Report the malaria status.
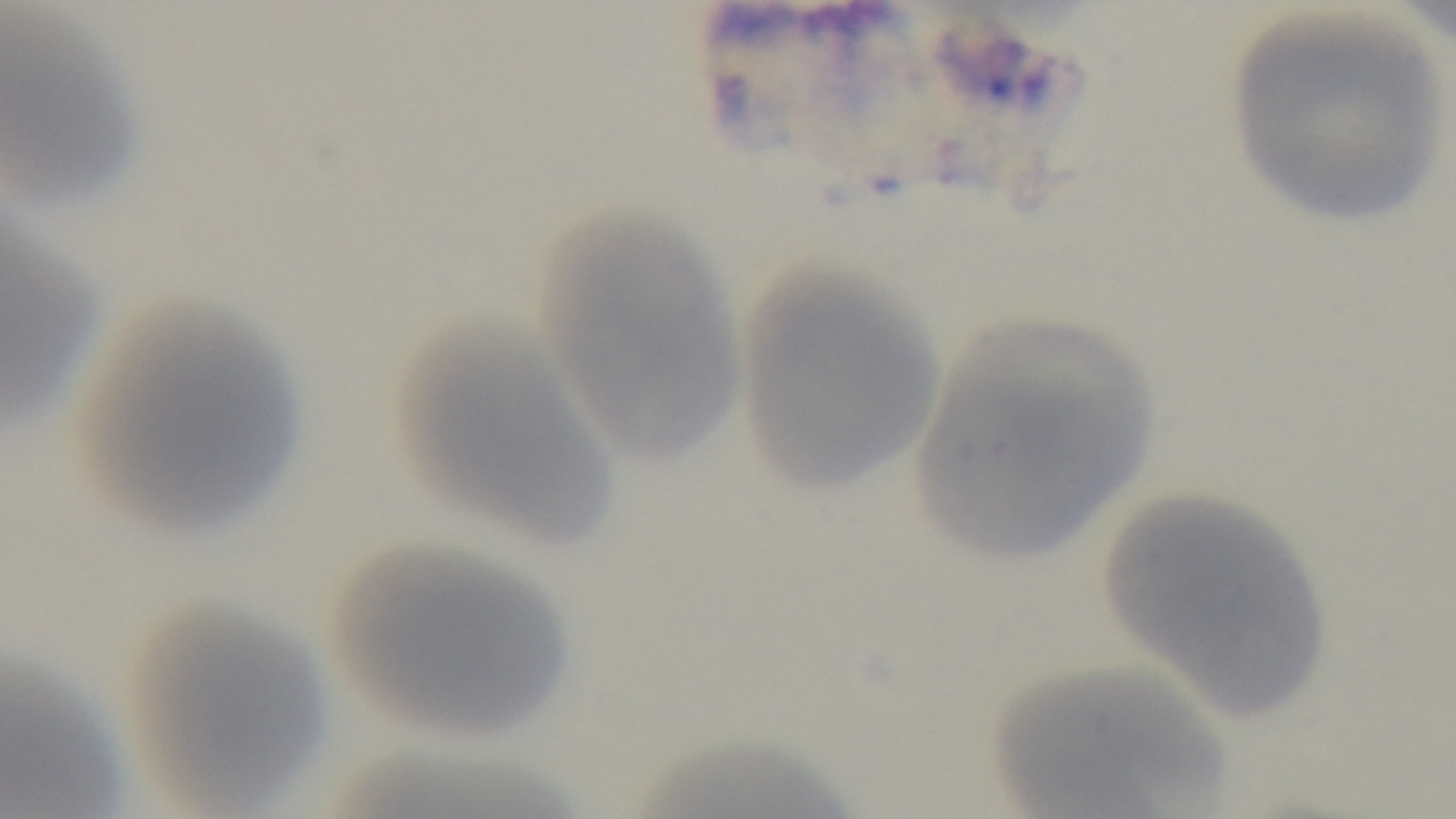

Uninfected.

Summary:
  - Modality: light microscopy
  - Preparation: thin smear
  - Capture: mounted 4K digital camera
  - Objective: 100x oil immersion
  - Stain: Giemsa
  - Field of view: single